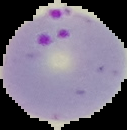
Result: Plasmodium parasites detected. From a thin blood film. The area outside the segmented cell region is set to black. Image is 127×130 pixels.